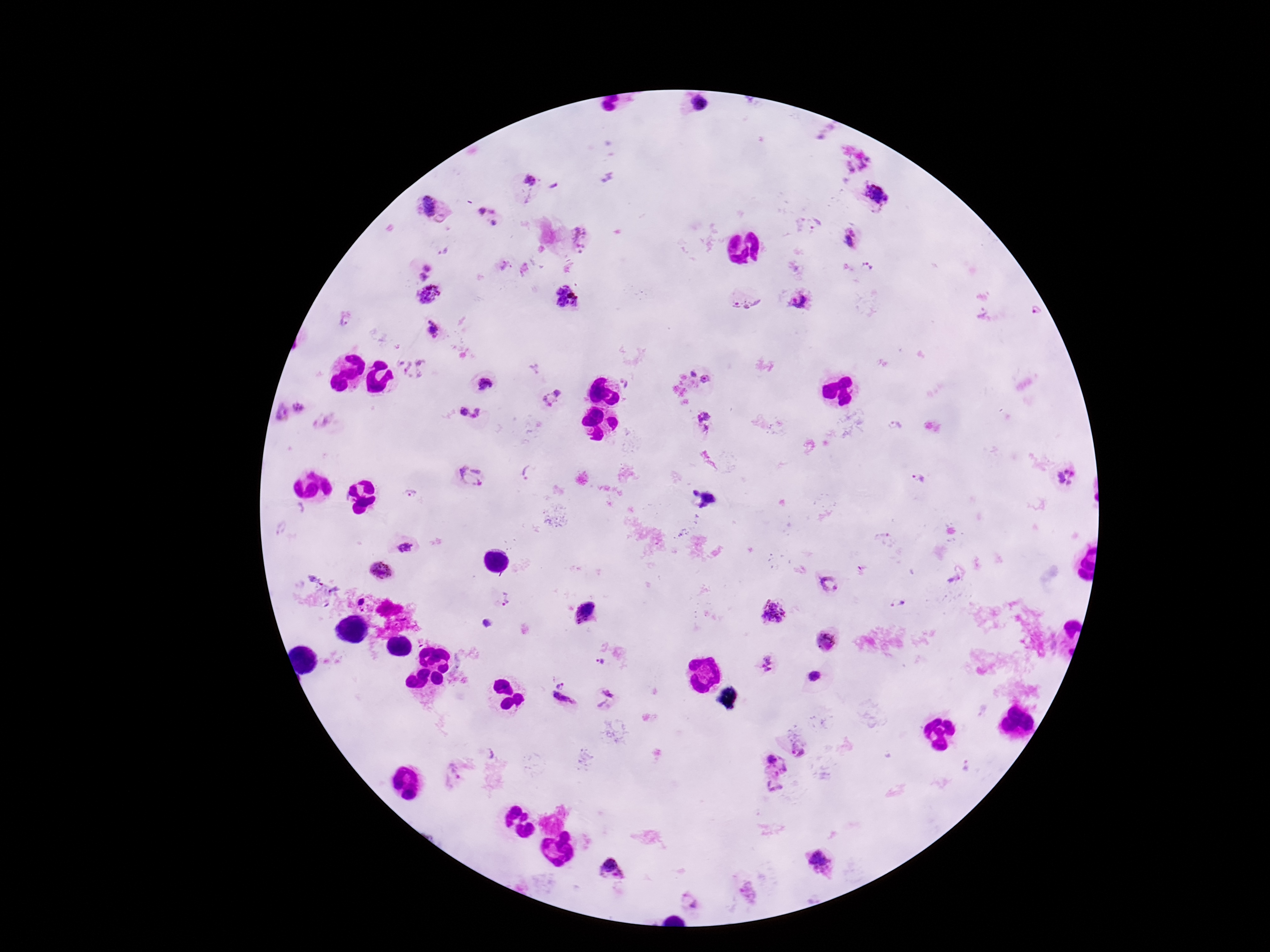
capture = smartphone camera through the microscope eyepiece
image size = 1270×952 pixels
field of view = single
stain = Giemsa
Plasmodium parasite locations = approximate centers as (x, y) in pixels: (700, 104), (532, 180), (877, 196), (431, 206), (487, 207), (495, 224), (816, 226), (584, 237), (855, 241), (506, 265), (865, 265), (430, 266), (422, 277), (428, 294), (566, 300), (804, 300), (740, 301), (1041, 311), (345, 322), (434, 327), (413, 368), (694, 371), (705, 379), (484, 384), (552, 397), (298, 407), (468, 413), (702, 414), (281, 415), (530, 472), (1065, 477), (469, 478), (917, 478), (695, 492), (407, 496), (710, 499), (406, 547), (382, 570), (829, 585), (504, 600), (362, 602), (899, 603), (777, 614), (487, 624), (828, 641), (599, 662), (766, 667), (560, 683), (608, 697), (560, 705), (800, 750), (773, 762), (453, 776), (774, 785), (822, 864), (611, 868), (688, 901)
magnification = 100x
patient malaria status = infected
preparation = thick peripheral-blood smear